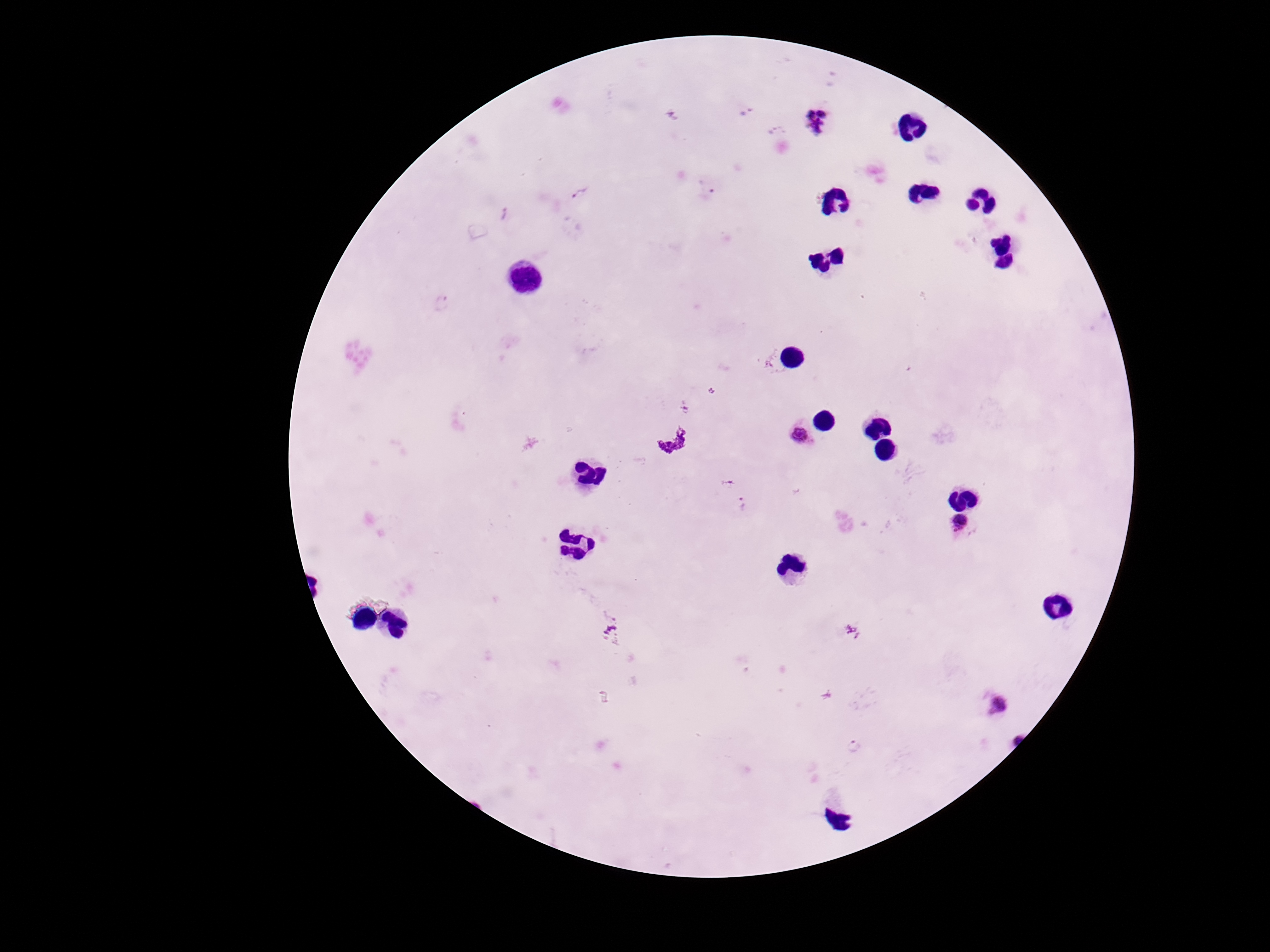
{
  "preparation": "thick blood smear",
  "plasmodium_parasite_locations": "approximate object centers, in pixels from the top-left corner: (x=747, y=111), (x=672, y=115), (x=817, y=123), (x=777, y=130), (x=707, y=187), (x=580, y=193), (x=504, y=215), (x=442, y=303), (x=711, y=390), (x=686, y=408), (x=800, y=435), (x=742, y=505), (x=959, y=523), (x=611, y=632), (x=1001, y=706)",
  "magnification": "100x",
  "image_size": "1270×952 pixels",
  "capture": "smartphone camera through the microscope eyepiece",
  "stain": "Giemsa",
  "patient_malaria_status": "positive",
  "field_of_view": "single"
}